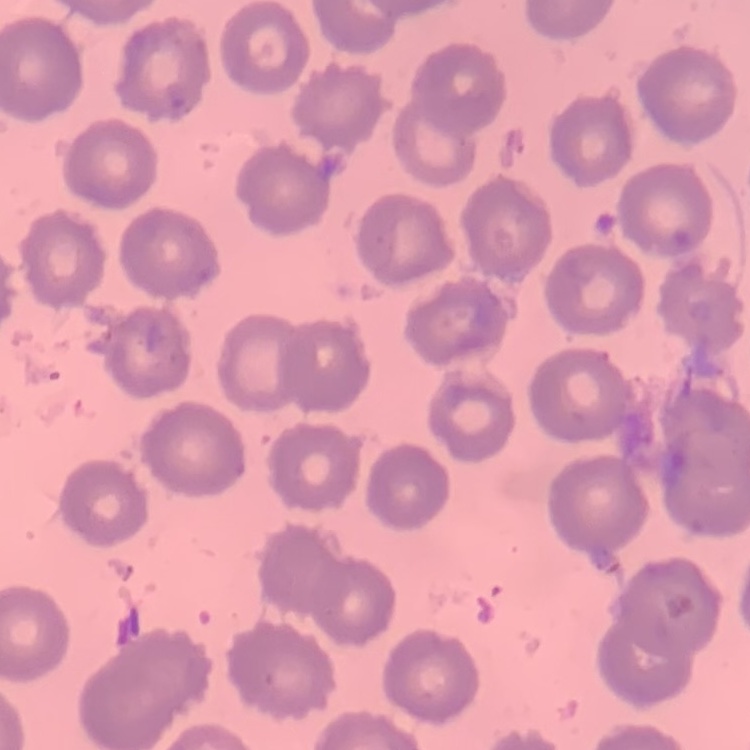

red blood cell morphology = no rouleaux formation
preparation = thin blood smear
image type = one tile cut from a larger photomicrograph
stain = Field's or Giemsa